Locate every Plasmodium parasite.
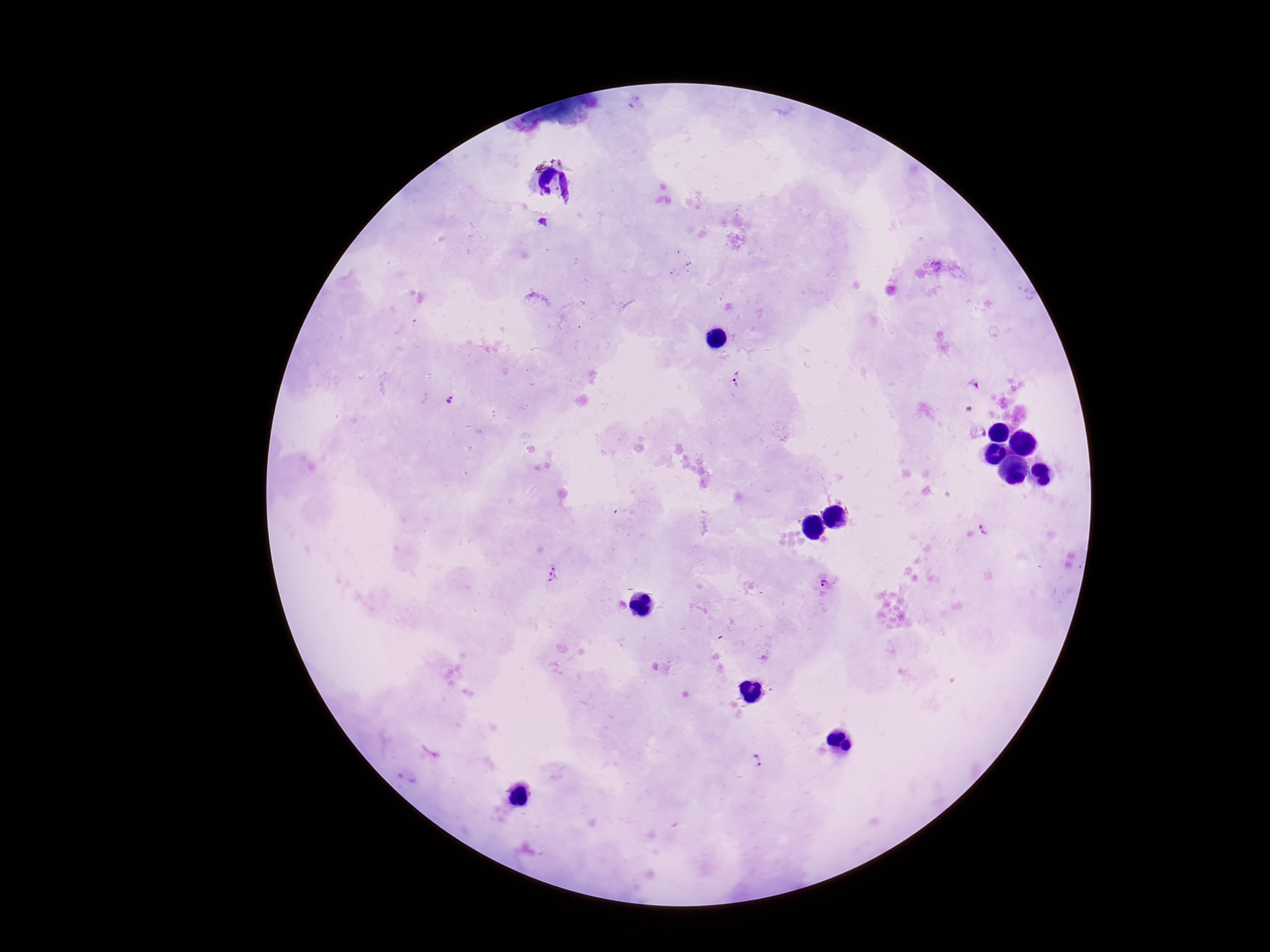
Approximate centers as {x, y} in pixels.
Plasmodium parasites: {543, 222}, {739, 378}, {973, 383}, {449, 400}, {975, 431}, {986, 527}, {552, 573}, {828, 586}, {753, 761}.

{
  "stain": "Giemsa",
  "capture": "smartphone camera through the microscope eyepiece",
  "magnification": "100x",
  "patient_malaria_status": "positive",
  "preparation": "thick blood smear",
  "image_size": "1270×952 pixels",
  "field_of_view": "one from this slide"
}